Assess the morphology of the erythrocytes.
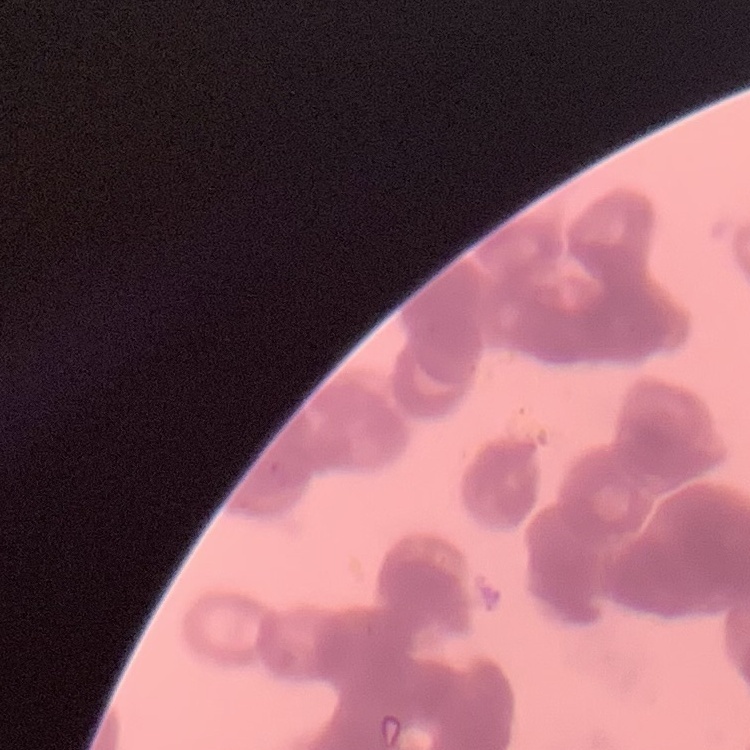
They show rouleaux formation.

Summary:
  - Stain: Field's or Giemsa
  - Preparation: thin blood film
  - Image type: one tile cut from a larger photomicrograph